Assess this cell for malaria.
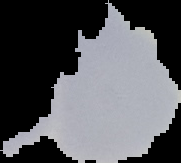
It is parasitized.

Summary:
  - Preparation: thin blood smear
  - Image type: segmented cell region on a black background
  - Image size: 181×163 pixels